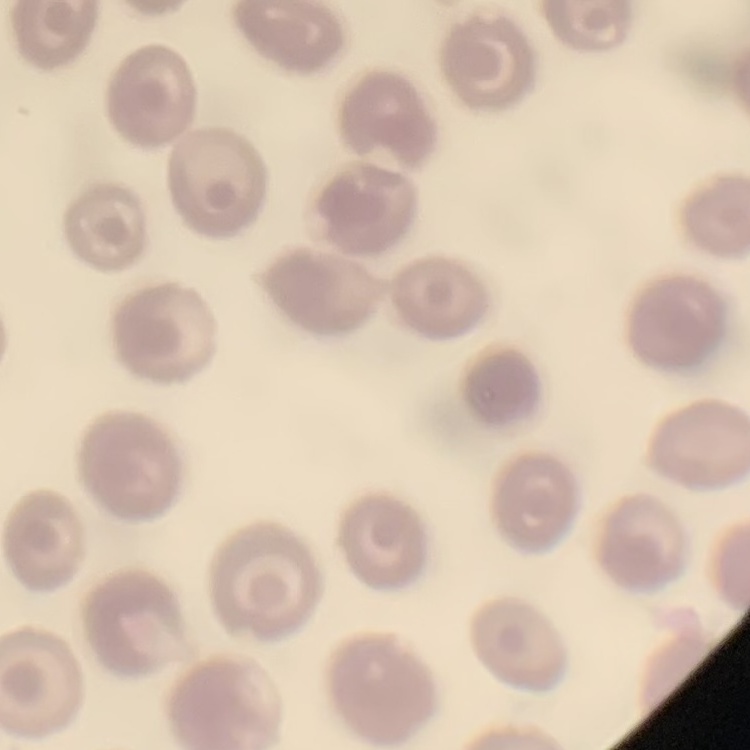 The red blood cells show no rouleaux formation. One tile cut from a larger photomicrograph. Field's or Giemsa stain. Thin peripheral smear.